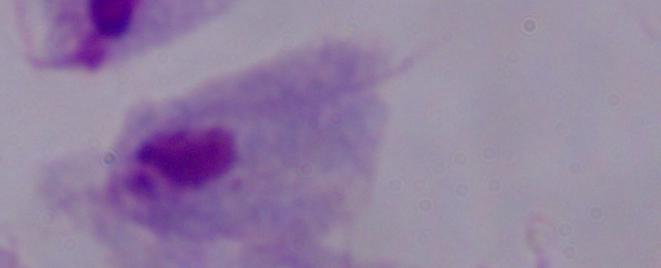

1000x magnification. Photomicrograph. A trichomonad is seen.